State the blood parasite species.
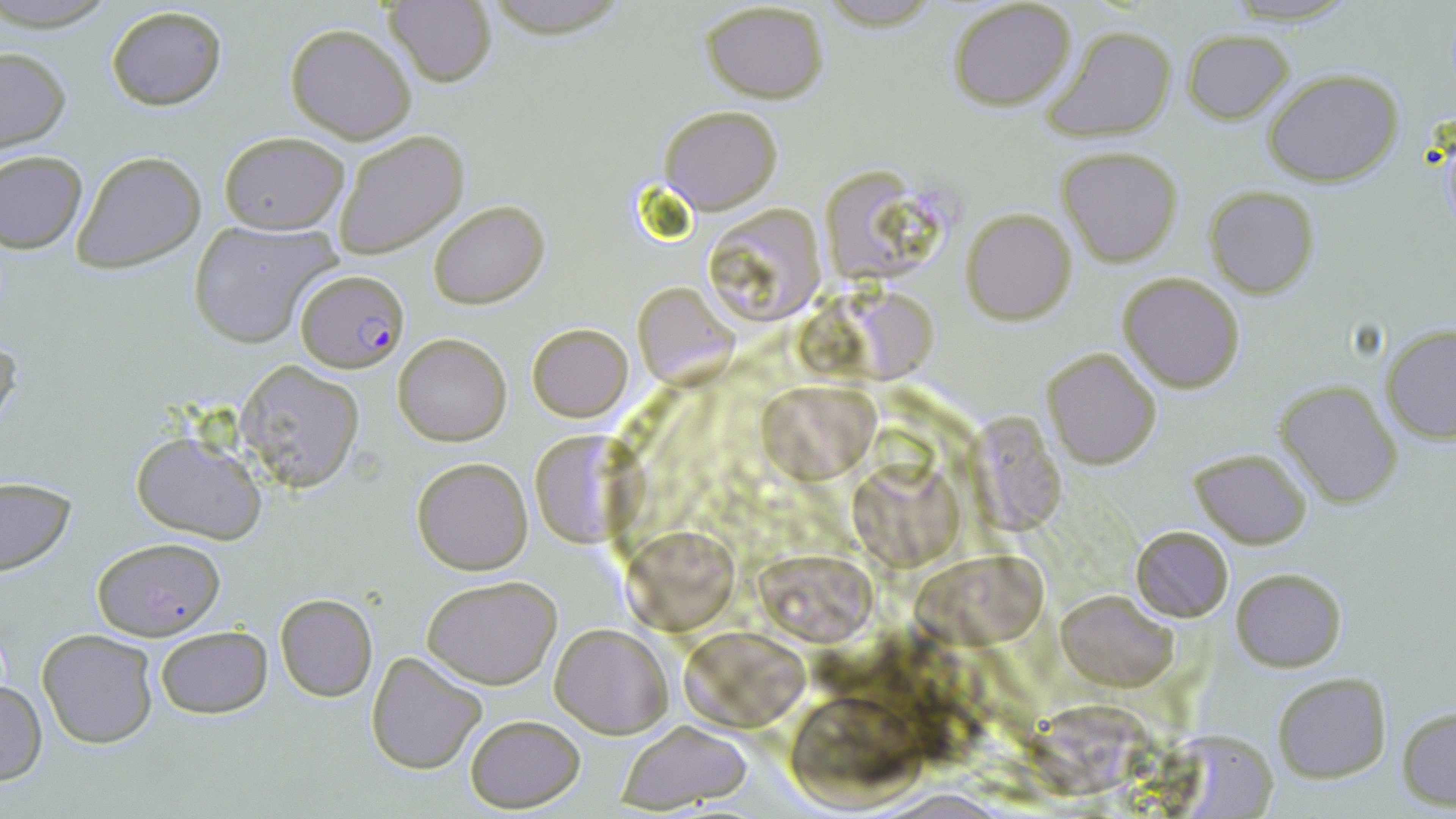

Plasmodium falciparum.

Approximate bounding boxes as (x1,y1)-(x2,y2) corner pairs in pixels. Uninfected red blood cell locations: (495,0)-(618,38), (828,0)-(936,35), (1221,0)-(1361,26), (383,1)-(498,88), (947,1)-(1077,112), (700,2)-(830,104), (106,5)-(227,112), (285,23)-(417,145), (1042,24)-(1177,143), (1183,29)-(1294,123), (0,47)-(72,155), (1263,69)-(1405,187), (660,104)-(782,214), (218,131)-(348,235), (335,131)-(467,259), (1058,146)-(1183,266), (0,150)-(87,254), (72,151)-(206,273), (818,163)-(938,278), (1205,187)-(1319,298), (429,200)-(548,309), (703,202)-(829,327), (962,207)-(1076,325), (189,220)-(337,349), (1117,272)-(1247,392), (633,283)-(736,385), (849,290)-(938,381), (526,322)-(633,422), (1380,324)-(1456,444), (0,333)-(20,441), (393,333)-(511,446), (1042,348)-(1162,469), (236,360)-(364,491), (1274,378)-(1404,508), (757,380)-(883,478), (970,408)-(1069,536), (129,429)-(265,543), (529,431)-(631,547), (1189,448)-(1313,546), (410,457)-(533,575), (849,459)-(963,572), (0,477)-(76,578), (625,525)-(739,631), (1130,525)-(1234,622), (90,537)-(227,639), (753,548)-(880,646), (912,550)-(1050,641), (1230,566)-(1346,672), (421,574)-(560,689), (1056,588)-(1178,691), (275,593)-(377,701), (550,622)-(673,737), (154,624)-(273,719), (37,629)-(158,749), (676,631)-(815,730), (365,652)-(486,775), (1272,674)-(1392,784), (0,680)-(46,785), (788,695)-(928,810), (1022,699)-(1165,802), (1398,707)-(1456,810), (463,714)-(583,812), (613,719)-(753,812). Plasmodium falciparum-infected red blood cell locations: (297,269)-(409,373). 1000x magnification. Image is 1456×819 pixels. One field of a larger specimen. Thin blood film. Light microscopy. May-Grünwald-Giemsa-stained preparation.